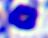
{
  "identification": "leukocyte",
  "magnification": "400x",
  "modality": "photomicrograph"
}